Outline each blood parasite and name the species.
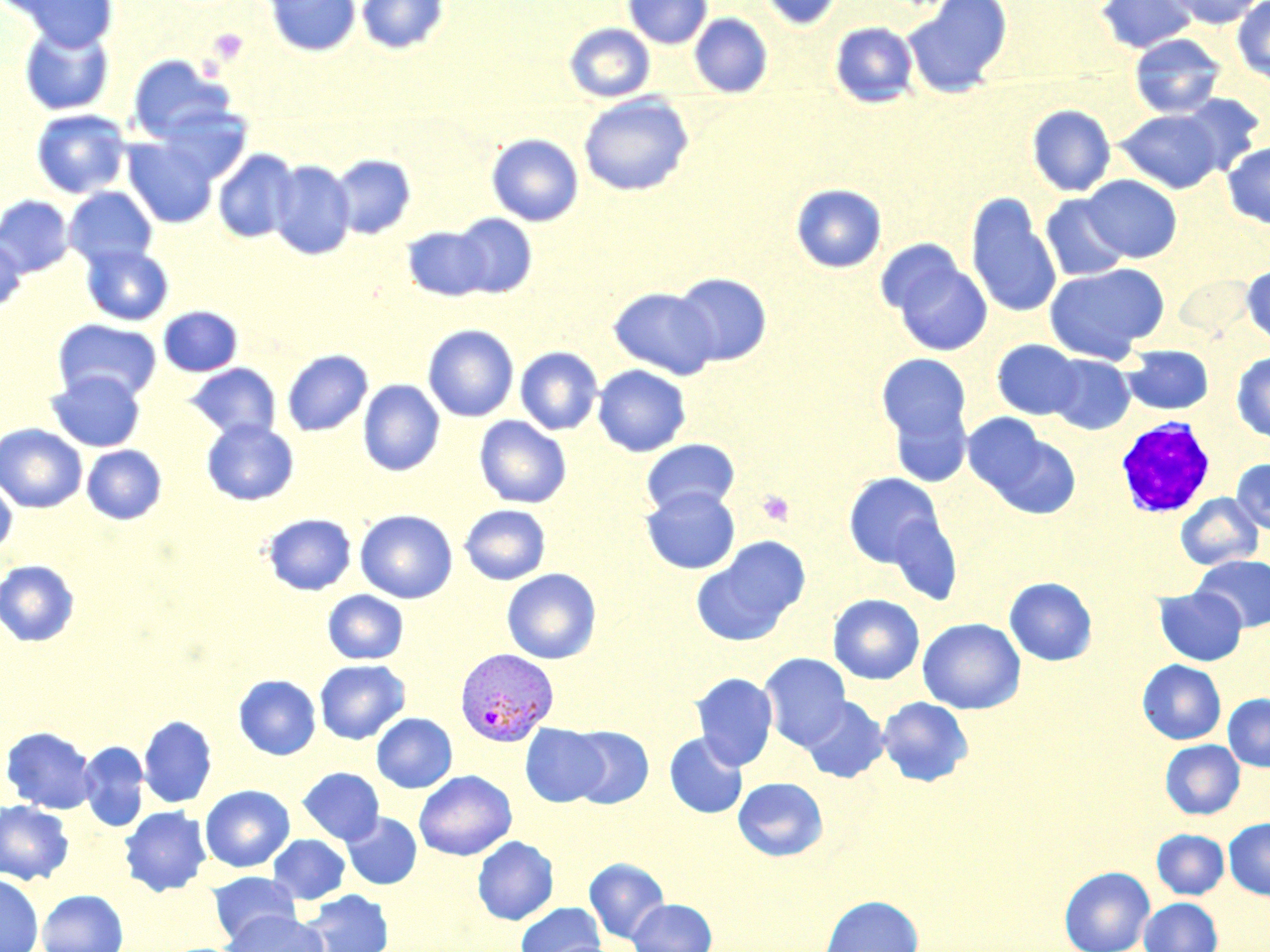

Approximate bounding boxes as [x1, y1, x2, y2] in pixels.
Plasmodium vivax-infected red blood cells: [455, 647, 559, 746].
No Plasmodium falciparum, Plasmodium ovale, Plasmodium malariae, Babesia divergens, or Trypanosoma brucei observed.

slide-level diagnosis = Plasmodium vivax
magnification = 1000x
field of view = single
image size = 1270×952 pixels
platelet locations = approximate bounding boxes as [x1, y1, x2, y2] in pixels: [208, 29, 249, 65], [757, 490, 794, 527]
white blood cell locations = approximate bounding boxes as [x1, y1, x2, y2] in pixels: [1115, 418, 1216, 518]
preparation = thin blood smear
modality = light microscopy
stain = May-Grünwald-Giemsa
uninfected red blood cell locations = approximate bounding boxes as [x1, y1, x2, y2] in pixels: [263, 0, 360, 56], [356, 0, 449, 55], [623, 0, 712, 49], [759, 0, 842, 31], [903, 0, 1013, 97], [1095, 0, 1198, 53], [1165, 0, 1266, 28], [12, 1, 119, 51], [1232, 1, 1270, 84], [690, 13, 772, 98], [830, 21, 918, 108], [564, 23, 655, 102], [20, 25, 114, 116], [1129, 33, 1226, 118], [128, 55, 235, 144], [578, 93, 694, 196], [1177, 93, 1265, 175], [156, 105, 254, 184], [1027, 105, 1115, 196], [31, 109, 131, 199], [1115, 109, 1224, 193], [486, 133, 583, 226], [123, 137, 218, 228], [1222, 141, 1270, 228], [213, 149, 299, 243], [330, 154, 416, 239], [268, 159, 355, 260], [1081, 175, 1182, 262], [790, 183, 886, 273], [64, 187, 157, 269], [966, 192, 1062, 318], [0, 195, 74, 278], [1040, 195, 1132, 282], [451, 214, 537, 297], [402, 226, 491, 300], [0, 237, 27, 314], [80, 244, 174, 326], [884, 250, 992, 357], [1043, 262, 1169, 363], [1241, 263, 1270, 347], [673, 272, 772, 366], [608, 287, 720, 379], [158, 306, 242, 376], [53, 319, 162, 403], [423, 324, 519, 421], [992, 339, 1085, 420], [1121, 345, 1214, 416], [515, 347, 603, 434], [281, 349, 373, 437], [877, 353, 972, 445], [1232, 353, 1270, 442], [1047, 354, 1135, 434], [185, 363, 281, 442], [593, 364, 691, 456], [46, 370, 146, 452], [358, 380, 444, 476], [888, 401, 972, 487], [474, 416, 571, 509], [966, 416, 1077, 514], [201, 419, 298, 505], [0, 424, 88, 513], [641, 439, 740, 516], [81, 445, 167, 524], [1231, 458, 1270, 534], [844, 472, 945, 569], [0, 476, 17, 557], [641, 486, 740, 574], [1176, 493, 1263, 570], [459, 504, 551, 584], [355, 509, 457, 603], [263, 513, 356, 595], [691, 537, 810, 646], [1192, 555, 1269, 631], [0, 560, 80, 647], [501, 568, 601, 664], [1004, 577, 1097, 666], [1154, 586, 1247, 665], [323, 590, 409, 664], [828, 594, 925, 684], [918, 617, 1025, 714], [759, 653, 851, 749], [314, 659, 410, 745], [1137, 660, 1226, 745], [691, 672, 778, 770], [233, 674, 321, 760], [1223, 693, 1270, 771], [800, 696, 890, 783], [878, 696, 973, 786], [372, 712, 457, 793], [139, 715, 217, 808], [521, 724, 609, 806], [1, 726, 97, 814], [566, 726, 654, 809], [664, 732, 748, 818], [1160, 740, 1244, 819], [78, 741, 150, 831], [297, 767, 384, 845], [414, 770, 517, 860], [733, 776, 828, 862], [200, 785, 295, 872], [0, 801, 73, 885], [119, 806, 212, 896], [341, 812, 422, 890], [1224, 817, 1270, 900], [1151, 829, 1229, 899], [268, 834, 351, 904], [472, 836, 559, 925], [584, 857, 670, 944], [1059, 866, 1154, 952], [208, 870, 300, 945], [0, 873, 43, 952], [37, 889, 128, 952], [300, 890, 393, 952], [819, 894, 923, 952], [1139, 897, 1223, 952], [628, 898, 716, 952], [516, 902, 605, 952], [220, 911, 328, 952]